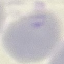
Summary:
  - Result: no malaria parasites seen
  - Stain: Giemsa
  - Capture: smartphone through the microscope eyepiece
  - Preparation: thin blood smear
  - Image type: cell patch, automatically extracted from a larger field of view and resized to 64 × 64 pixels